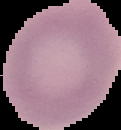

Summary:
  - Malaria status: uninfected
  - Preparation: thin blood smear
  - Image size: 121×130 pixels
  - Image type: segmented cell region on a black background